Name the parasite shown.
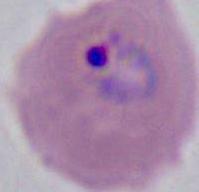

Plasmodium.

Photomicrograph. Captured at either 400x or 1000x magnification.